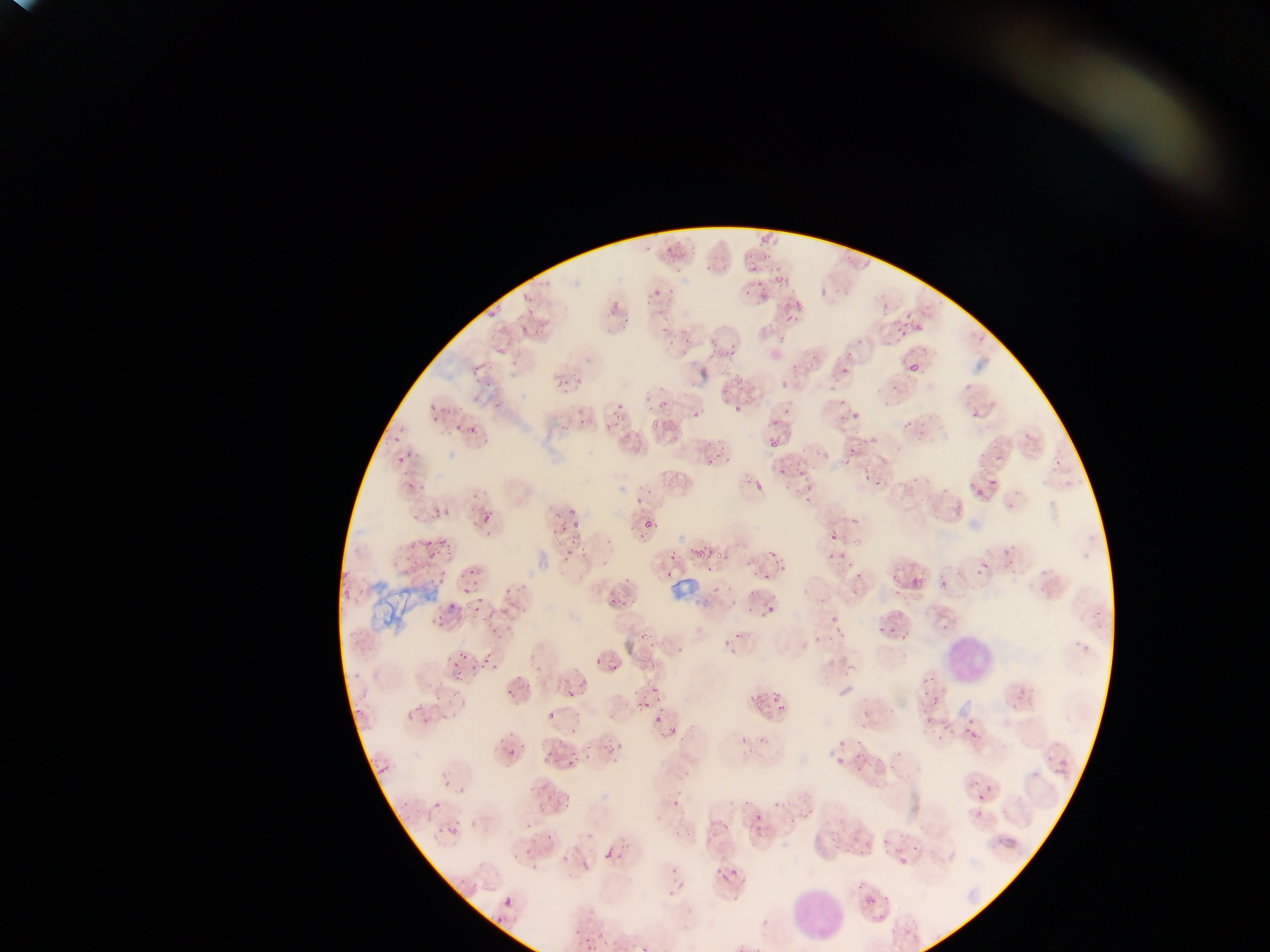

Approximate bounding boxes as {left, top, right, bottom} in pixels. Leukocyte locations: {941, 633, 997, 689}, {782, 886, 849, 947}. Malaria parasite locations: {751, 229, 782, 257}, {697, 248, 734, 277}, {645, 274, 674, 306}, {738, 276, 775, 302}, {602, 280, 634, 326}, {483, 301, 512, 317}, {777, 303, 798, 319}, {887, 317, 914, 339}, {646, 319, 686, 355}, {485, 328, 525, 355}, {702, 339, 729, 357}, {832, 352, 858, 374}, {902, 359, 929, 385}, {781, 373, 797, 387}, {555, 375, 568, 392}, {727, 388, 755, 412}, {971, 390, 987, 419}, {835, 392, 861, 422}, {427, 399, 444, 421}, {564, 399, 596, 434}, {603, 400, 631, 434}, {450, 413, 480, 432}, {645, 413, 673, 430}, {767, 421, 797, 450}, {841, 438, 863, 464}, {703, 439, 722, 462}, {388, 451, 411, 465}, {964, 452, 1009, 507}, {791, 456, 818, 482}, {855, 457, 897, 488}, {742, 464, 771, 494}, {401, 470, 428, 493}, {918, 473, 952, 501}, {555, 487, 592, 535}, {436, 495, 467, 515}, {476, 503, 499, 533}, {643, 521, 654, 532}, {826, 527, 843, 546}, {417, 533, 440, 550}, {754, 536, 795, 577}, {699, 538, 726, 568}, {424, 542, 450, 566}, {563, 543, 575, 567}, {974, 545, 1008, 576}, {669, 554, 677, 562}, {836, 568, 867, 606}, {906, 572, 926, 596}, {463, 576, 480, 595}, {601, 579, 627, 600}, {753, 580, 785, 617}, {943, 580, 950, 590}, {341, 590, 358, 612}, {464, 600, 482, 617}, {872, 605, 895, 640}, {432, 610, 448, 624}, {484, 610, 505, 636}, {815, 620, 840, 643}, {456, 648, 468, 665}, {478, 652, 496, 670}, {598, 654, 620, 673}, {452, 669, 459, 678}, {562, 675, 585, 696}, {635, 678, 665, 716}, {758, 680, 791, 725}, {431, 687, 446, 703}, {922, 695, 941, 730}, {353, 699, 370, 724}, {403, 701, 429, 722}, {536, 701, 559, 731}, {655, 705, 678, 738}, {955, 713, 989, 746}, {830, 737, 853, 769}, {505, 739, 532, 758}, {546, 746, 563, 763}, {563, 757, 575, 772}, {376, 762, 387, 776}, {538, 777, 553, 795}, {443, 780, 452, 789}, {964, 785, 981, 811}, {434, 802, 443, 812}, {746, 805, 771, 825}, {876, 818, 906, 860}, {834, 821, 863, 858}, {525, 831, 548, 856}, {599, 838, 620, 856}, {714, 854, 739, 884}, {862, 868, 892, 905}, {503, 896, 515, 909}, {892, 926, 906, 938}, {572, 932, 597, 952}. One field of view. Collected in Ghana. Thin blood smear. Photographed through a microscope with a mobile-phone camera. Image is 1270×952 pixels.